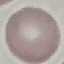
result = no malaria parasites detected
preparation = thin smear
image type = automatically extracted cell patch, resized to 64 × 64 pixels
stain = Giemsa
capture = smartphone camera at the microscope eyepiece